Give the extent of all uninfected red blood cells.
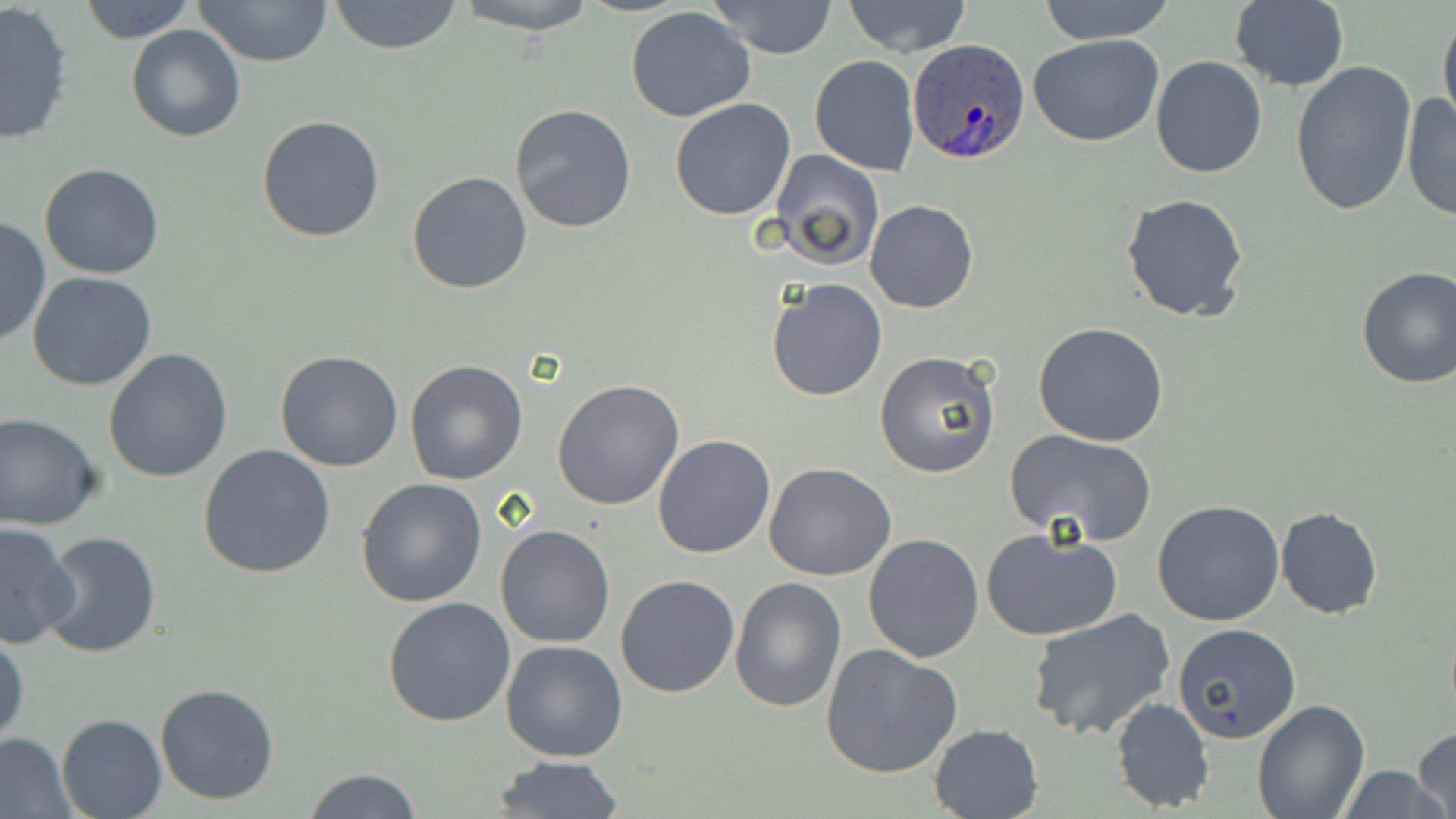
Approximate bounding boxes as [x1, y1, x2, y2] in pixels.
Uninfected red blood cells: [193, 0, 333, 68], [328, 0, 463, 55], [454, 0, 600, 33], [710, 0, 838, 58], [74, 1, 199, 43], [841, 1, 971, 56], [1033, 1, 1179, 43], [1227, 1, 1350, 91], [0, 2, 76, 145], [625, 5, 756, 123], [1438, 5, 1456, 130], [126, 24, 246, 142], [1028, 34, 1166, 147], [810, 55, 920, 175], [1150, 55, 1269, 178], [1290, 61, 1419, 220], [1400, 92, 1456, 224], [670, 98, 798, 220], [511, 104, 637, 232], [257, 116, 386, 242], [767, 148, 884, 270], [39, 162, 164, 279], [406, 171, 532, 295], [1122, 192, 1251, 325], [866, 200, 977, 313], [0, 215, 50, 348], [1354, 265, 1456, 388], [27, 271, 158, 391], [765, 277, 888, 402], [1033, 321, 1169, 447], [103, 348, 234, 483], [875, 350, 1002, 479], [275, 351, 404, 472], [405, 359, 528, 484], [552, 378, 684, 510], [0, 413, 103, 530], [1004, 429, 1159, 545], [653, 434, 774, 558], [197, 444, 337, 579], [764, 463, 896, 582], [356, 477, 488, 608], [1152, 499, 1285, 627], [1275, 507, 1384, 620], [0, 521, 78, 648], [495, 525, 615, 648], [980, 527, 1123, 642], [41, 531, 162, 659], [863, 533, 983, 664], [615, 574, 742, 698], [729, 577, 846, 713], [383, 595, 516, 726], [1026, 610, 1175, 740], [1171, 624, 1302, 744], [1, 630, 28, 748], [500, 639, 627, 762], [821, 643, 962, 779], [153, 682, 281, 805], [1110, 697, 1215, 815], [1251, 700, 1370, 819], [57, 714, 166, 819], [929, 723, 1044, 817], [1411, 728, 1455, 819], [1, 732, 74, 817], [492, 756, 626, 817], [1334, 764, 1452, 819], [305, 767, 421, 819].

Summary:
  - Plasmodium ovale-infected red blood cell locations: [907, 39, 1032, 163]
  - Slide-level diagnosis: Plasmodium ovale
  - Image size: 1456×819 pixels
  - Magnification: 1000x
  - Preparation: thin blood smear
  - Stain: May-Grünwald-Giemsa
  - Modality: optical microscopy
  - Field of view: one of a larger specimen